Report the malaria status.
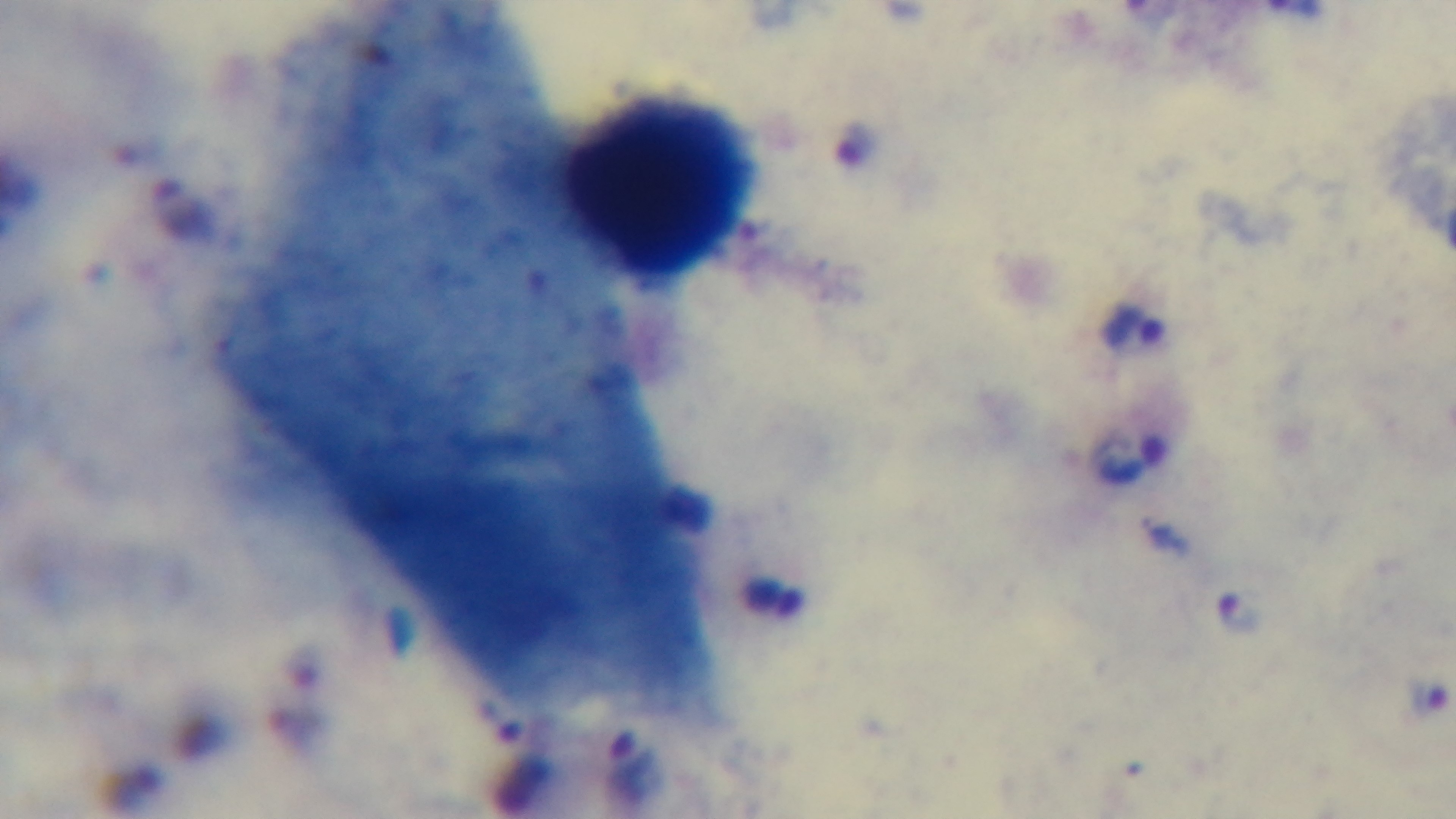
Infected.

capture = mounted 4K digital camera
preparation = thick blood film
field of view = one from the slide
modality = light microscopy
stain = Giemsa
objective = 100x oil immersion